Report the malaria status of this cell.
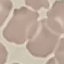

It is uninfected.

Thin blood film. Giemsa stain. Acquired by smartphone through the microscope eyepiece. Cell patch, automatically extracted from a larger field of view and resized to 64 × 64 pixels.